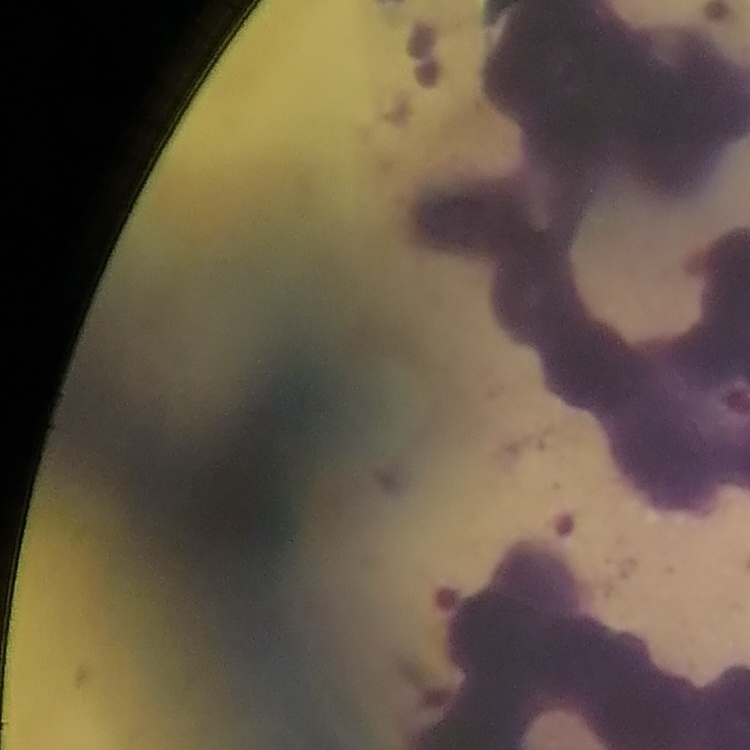
Summary:
  - Red blood cell morphology: rouleaux formation
  - Image type: square crop of a larger photomicrograph
  - Preparation: thin peripheral smear
  - Stain: Field's or Giemsa